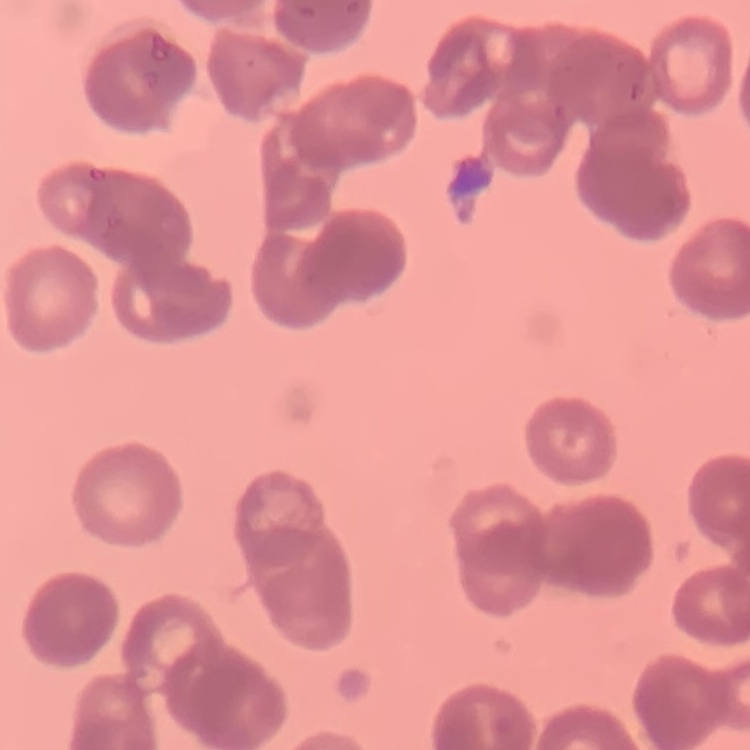

{
  "erythrocyte_morphology": "rouleaux formation",
  "image_type": "square crop of a larger photomicrograph",
  "preparation": "thin blood smear",
  "stain": "Field's or Giemsa"
}